Describe the morphology of the red blood cells.
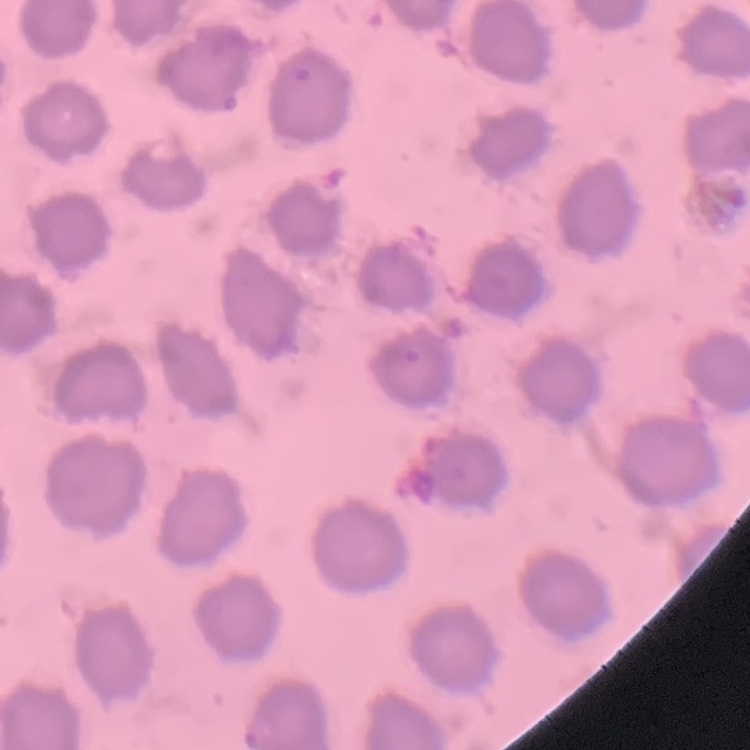

No rouleaux formation.

Stained with either Field's or Giemsa. Thin peripheral smear. One tile cut from a larger photomicrograph.